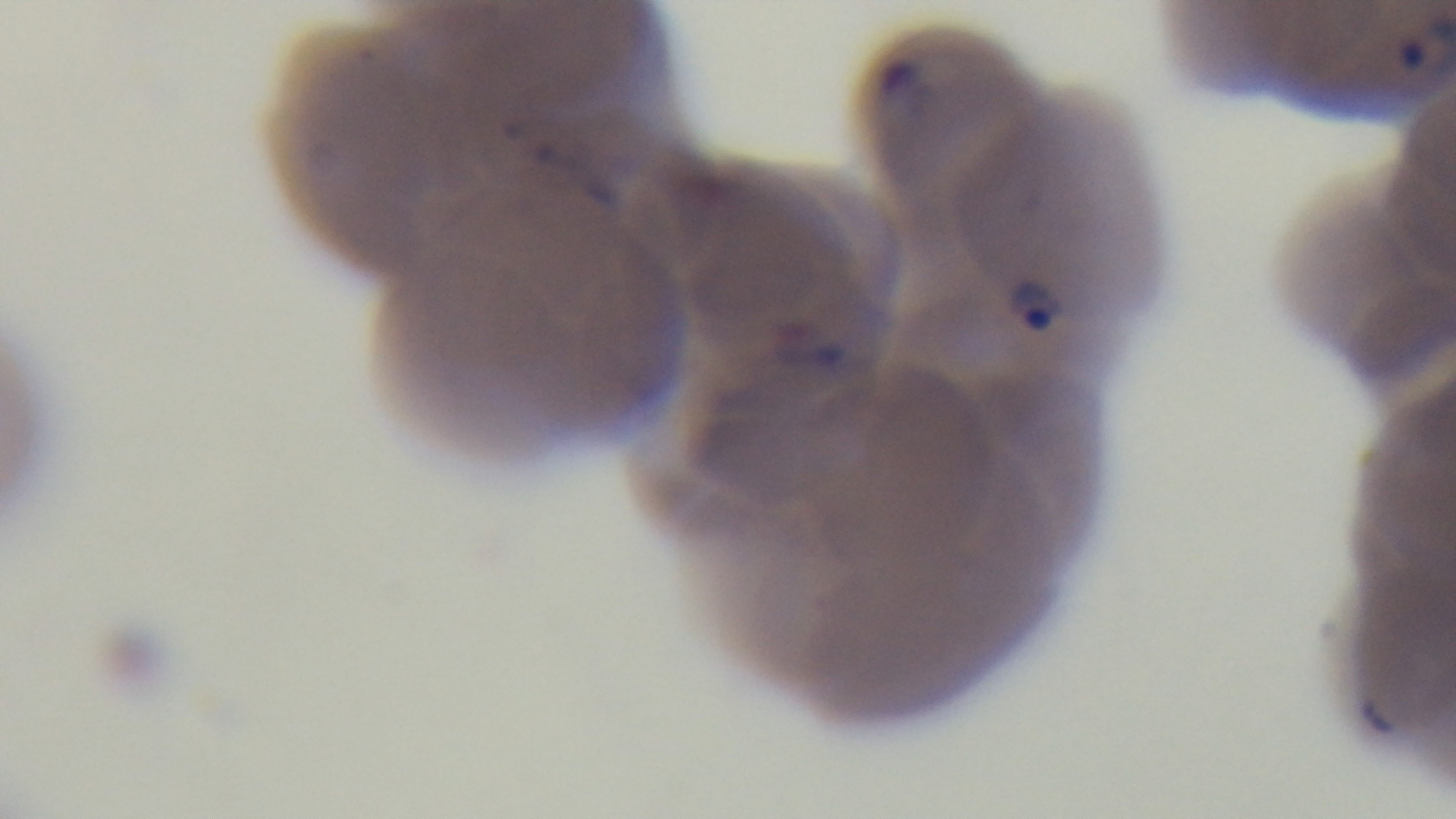

Preparation: thin blood film. 100x oil-immersion objective. Giemsa stain. One field from the slide. Malaria status: infected. Light microscopy. Mounted 4K digital camera.